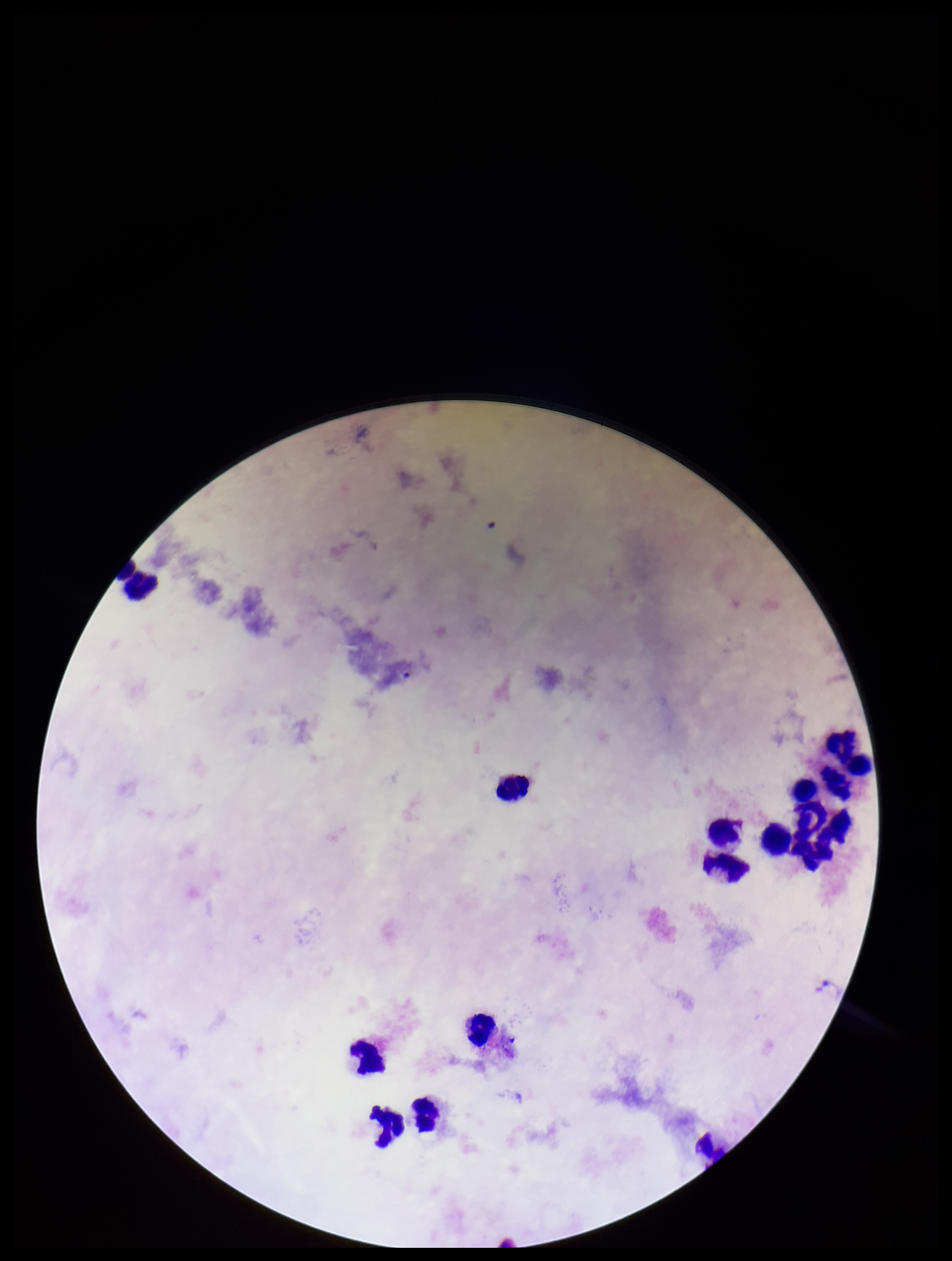

field of view = one from this slide
patient malaria status = negative
capture = smartphone photograph through the microscope eyepiece
image size = 952×1261 pixels
leukocyte count = 13
parasite count = 0
stain = Giemsa
preparation = thick blood smear
Plasmodium parasites = none seen